Assess this cell for malaria.
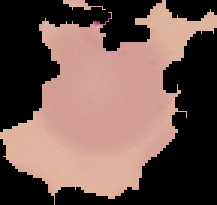
It is parasitized.

Summary:
  - Preparation: thin blood smear
  - Image type: segmented cell region on a black background
  - Image size: 217×205 pixels